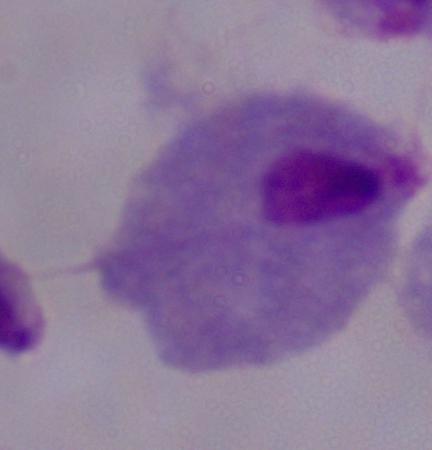

Summary:
  - Magnification: 1000x
  - Identification: trichomonad
  - Modality: photomicrograph